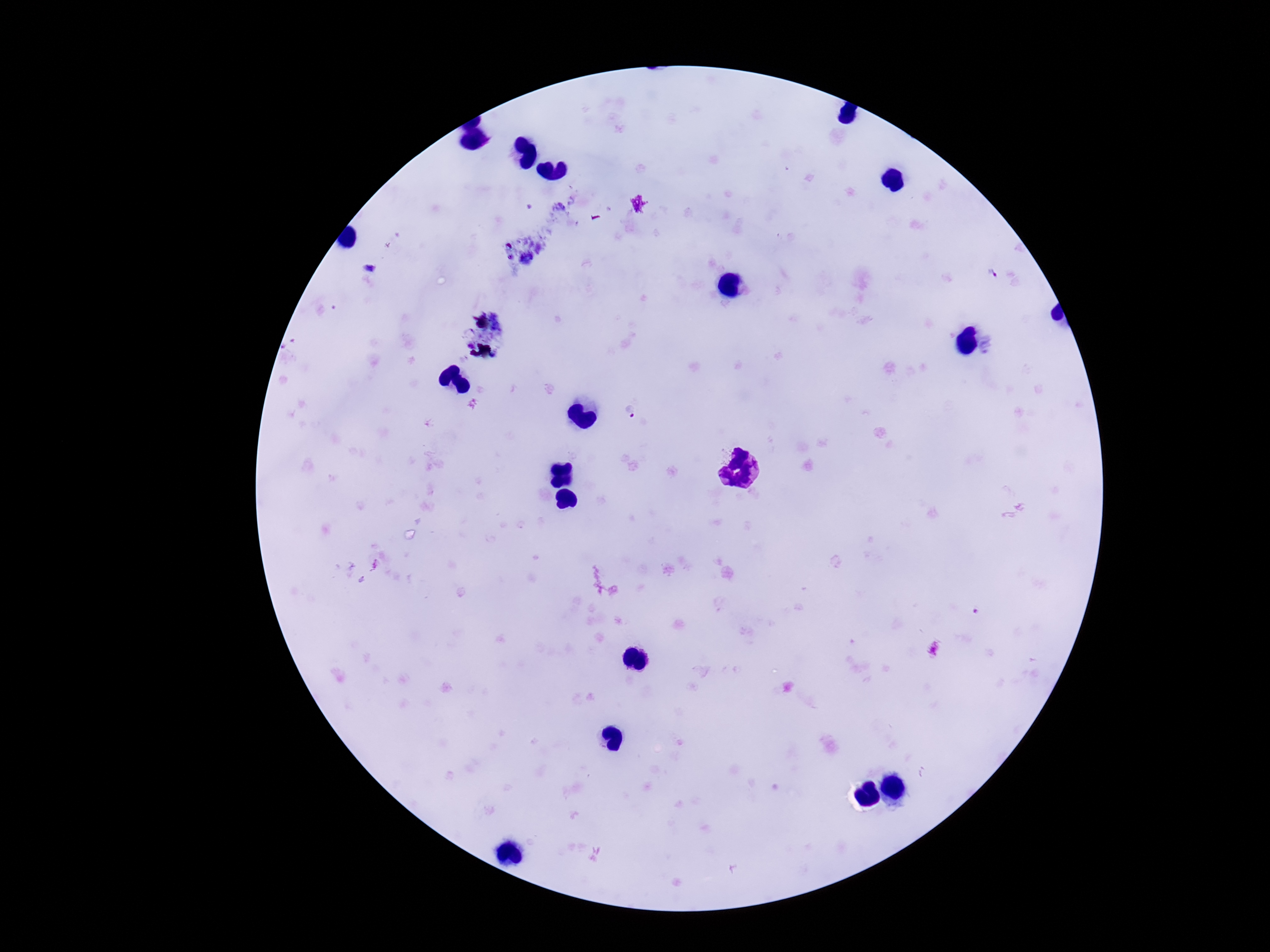 Approximate centers as {x, y} in pixels. Plasmodium parasite locations: {993, 275}, {630, 411}. Image is 1270×952 pixels. 100x magnification. Smartphone photograph taken through the microscope eyepiece. Giemsa-stained preparation. Single field of view. Patient malaria status: infected. Thick blood film.